Point out each Plasmodium parasite.
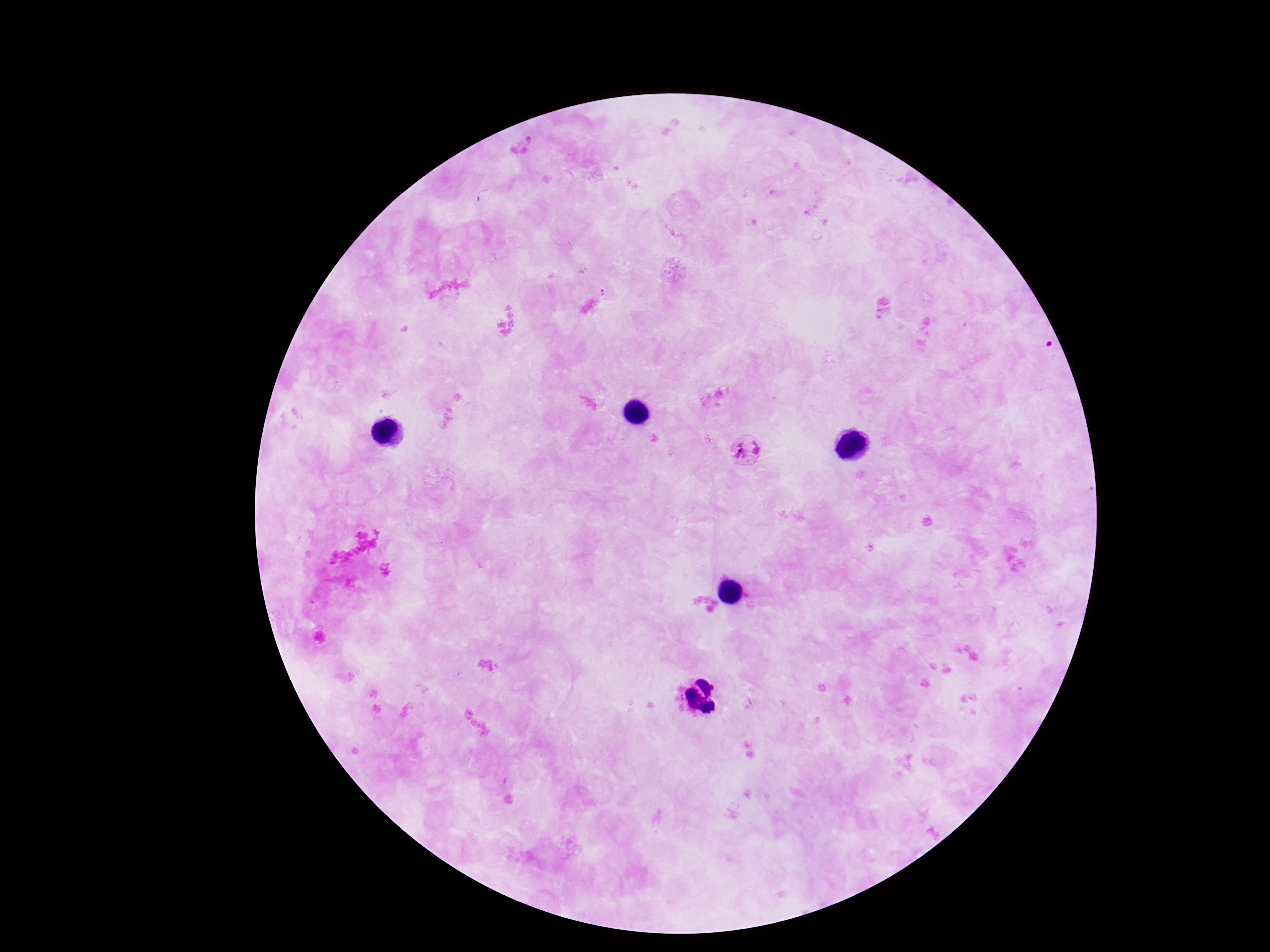
Approximate centers as {x, y} in pixels.
Plasmodium parasites: {751, 451}.

Giemsa-stained preparation. Thick peripheral-blood smear. Patient malaria status: positive. One field from this slide. Smartphone photograph taken through the microscope eyepiece. 100x magnification. Image is 1270×952 pixels.